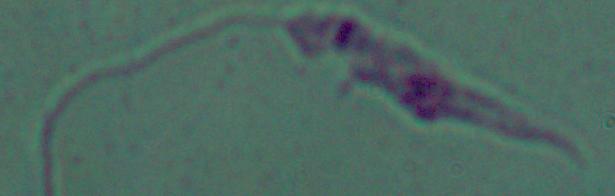

modality: photomicrograph
identification: Leishmania
magnification: 1000x